Point out each malaria parasite.
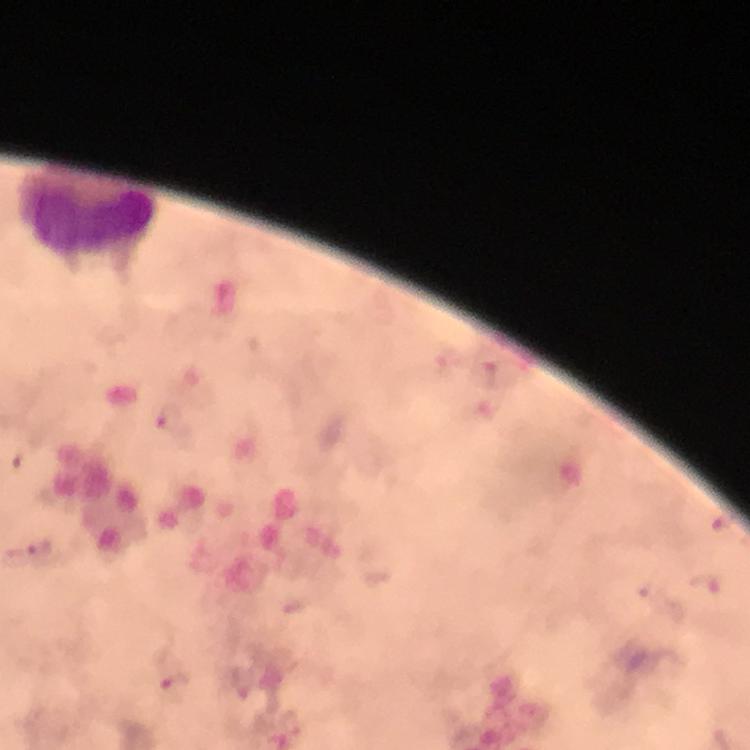

Approximate centers as [x, y] in pixels.
Malaria parasites: [175, 688].

capture = smartphone mounted on the microscope
context = from a malaria diagnostic workup
cropped from = a single field of view
stain = Giemsa
immersion oil = used
magnification = 100x
preparation = thick blood film
leukocyte locations = approximate centers as [x, y] in pixels: [87, 218]
image size = 750×750 pixels